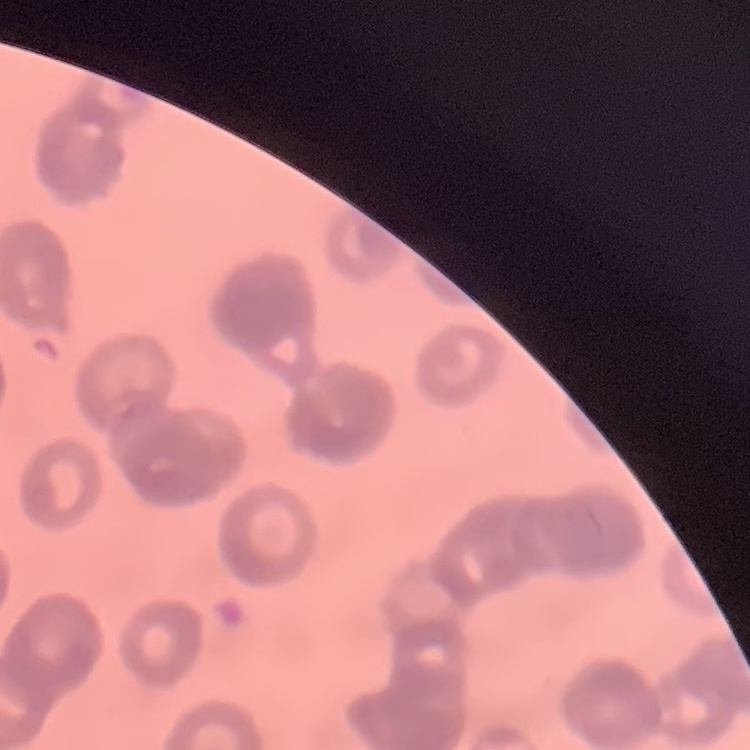

Summary:
  - Red blood cell morphology: rouleaux formation
  - Stain: Field's or Giemsa
  - Image type: one tile cut from a larger photomicrograph
  - Preparation: thin blood smear